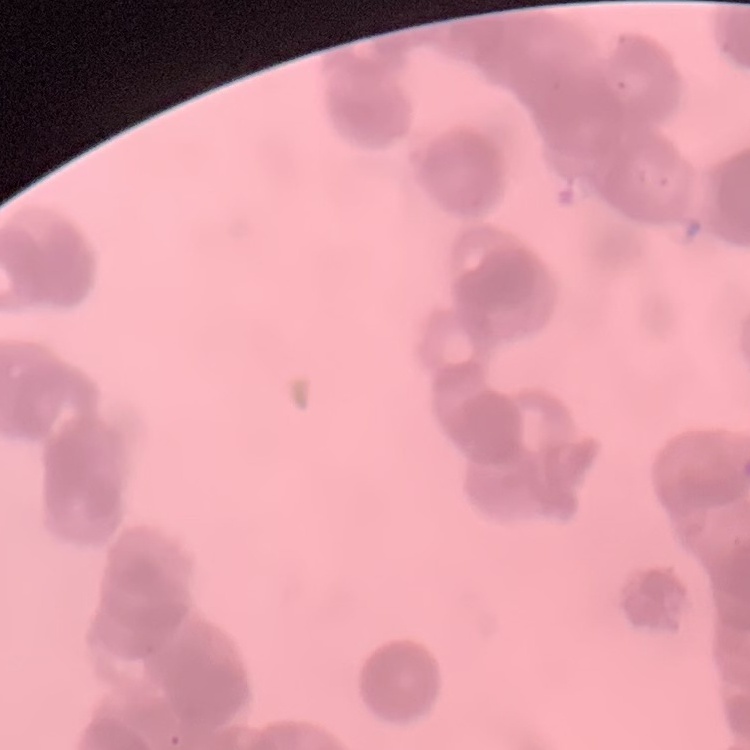
Summary:
  - Erythrocyte morphology: rouleaux formation
  - Image type: square crop of a larger photomicrograph
  - Stain: Field's or Giemsa
  - Preparation: thin peripheral smear